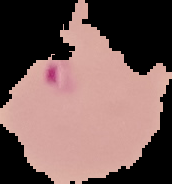
image_type: segmented cell region on a black background
image_size: 172×184 pixels
result: Plasmodium parasites identified
preparation: thin blood film